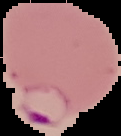

Result: Plasmodium parasites detected. The area outside the segmented cell region is set to black. Image is 121×136 pixels. From a thin blood smear.